Locate every blood parasite and identify its species.
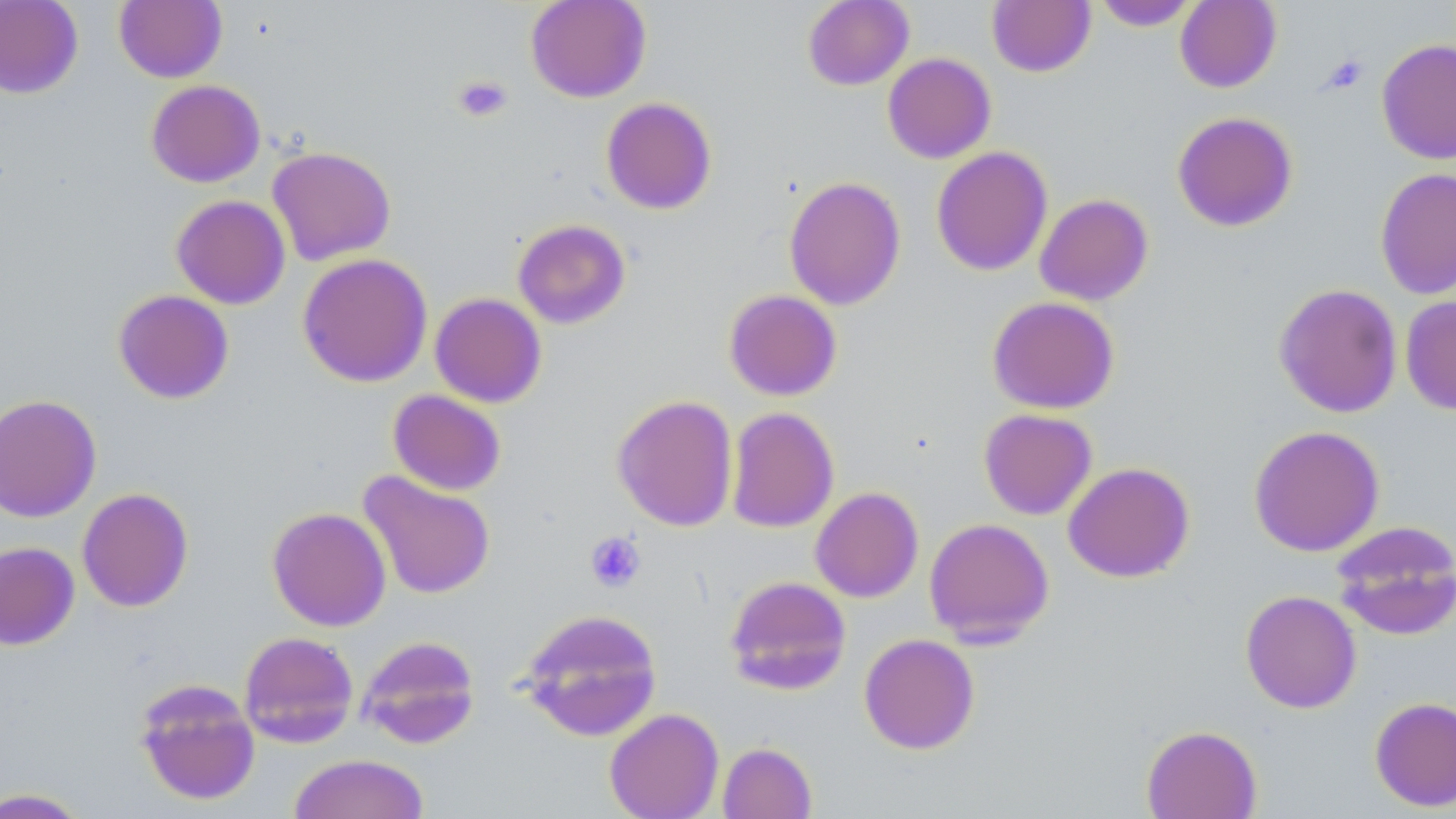
No blood parasites seen.

slide-level diagnosis = no evidence of blood parasites
magnification = 1000x
preparation = thin blood film
platelet locations = approximate bounding boxes as [x1, y1, x2, y2] in pixels: [1322, 55, 1368, 93], [452, 74, 513, 124], [585, 531, 646, 592]
field of view = one of a larger specimen
modality = light microscopy
image size = 1456×819 pixels
stain = May-Grünwald-Giemsa
uninfected red blood cell locations = approximate bounding boxes as [x1, y1, x2, y2] in pixels: [0, 0, 83, 99], [114, 0, 227, 83], [525, 0, 652, 103], [802, 0, 915, 90], [986, 0, 1096, 78], [1175, 0, 1281, 93], [1092, 1, 1201, 31], [1376, 40, 1456, 165], [882, 53, 996, 164], [146, 79, 265, 187], [600, 97, 717, 215], [1172, 111, 1298, 232], [267, 146, 396, 266], [931, 146, 1053, 276], [1375, 167, 1456, 300], [783, 175, 906, 310], [1034, 193, 1153, 306], [171, 195, 290, 309], [512, 219, 631, 329], [297, 253, 433, 388], [1274, 283, 1403, 418], [113, 289, 234, 404], [723, 289, 842, 401], [430, 292, 547, 408], [1400, 295, 1456, 416], [987, 296, 1120, 414], [387, 389, 506, 496], [0, 393, 101, 523], [611, 394, 739, 532], [725, 406, 839, 533], [978, 408, 1097, 520], [1248, 425, 1385, 557], [1063, 462, 1195, 583], [358, 471, 496, 600], [810, 486, 924, 603], [77, 487, 194, 612], [267, 506, 391, 632], [924, 517, 1055, 647], [1330, 521, 1456, 640], [0, 541, 80, 650], [724, 575, 851, 695], [1240, 590, 1362, 714], [517, 608, 662, 741], [238, 631, 358, 748], [859, 633, 980, 755], [356, 635, 481, 749], [134, 677, 261, 806], [1369, 696, 1456, 812], [604, 707, 724, 819], [1141, 724, 1262, 819], [717, 741, 817, 819], [289, 753, 430, 819], [0, 787, 91, 818]